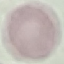
malaria status = uninfected
stain = Giemsa
preparation = thin blood film
image type = automatically extracted cell patch, resized to 64 × 64 pixels
capture = smartphone camera at the microscope eyepiece